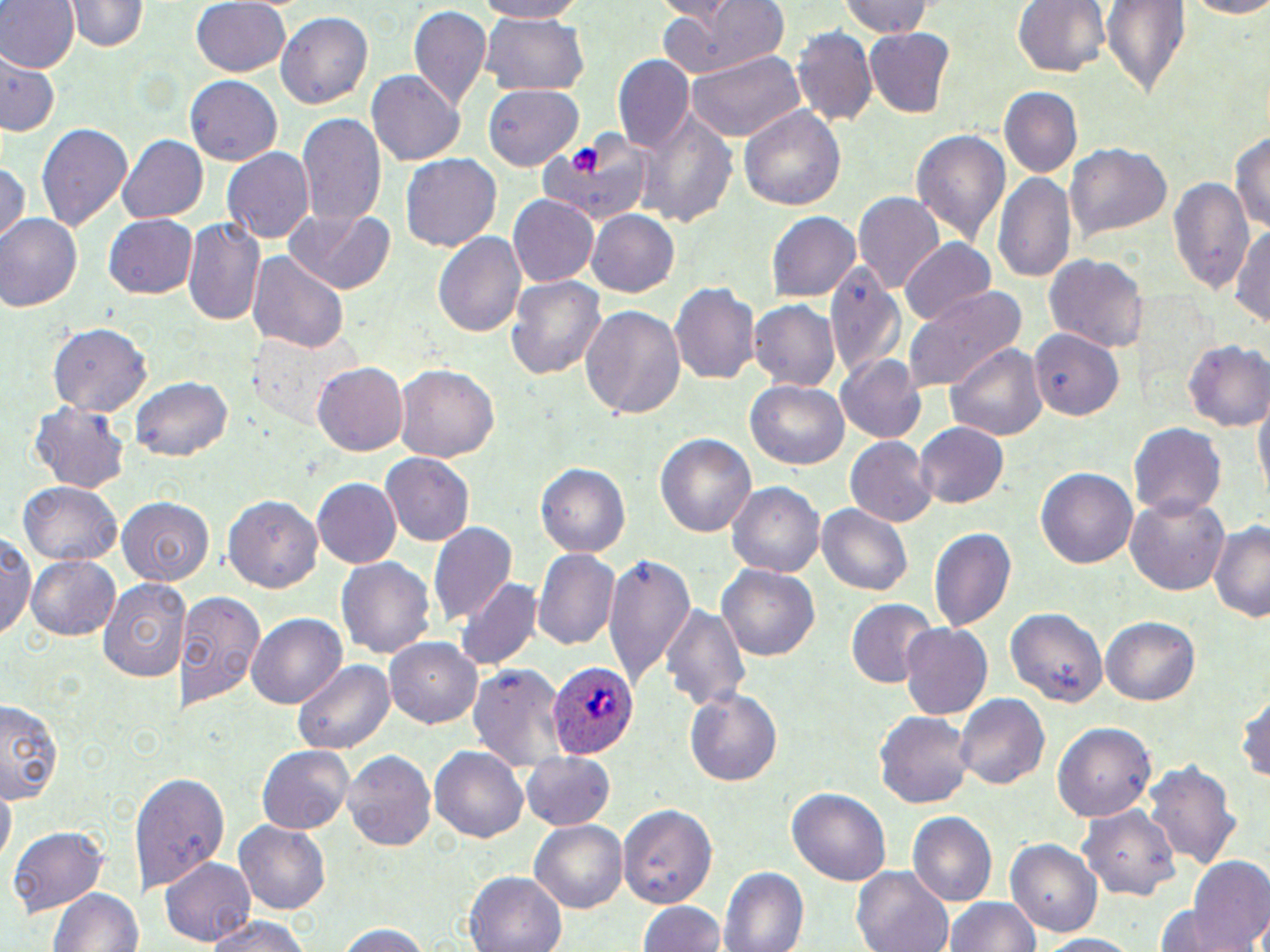

Summary:
  - Coordinate format: approximate bounding boxes as (x1, y1, x2, y2) in pixels
  - Platelet locations: (571, 144, 603, 176)
  - Plasmodium ovale-infected red blood cell locations: (546, 659, 638, 756)
  - Uninfected red blood cell locations: (0, 0, 78, 74), (65, 0, 150, 54), (193, 0, 292, 76), (473, 0, 590, 22), (837, 0, 934, 40), (1012, 0, 1108, 79), (1173, 0, 1270, 17), (1101, 1, 1192, 101), (655, 2, 792, 77), (408, 6, 493, 113), (276, 11, 372, 111), (479, 13, 587, 92), (793, 26, 878, 127), (865, 29, 956, 118), (684, 48, 808, 141), (614, 56, 695, 154), (3, 57, 58, 136), (367, 69, 466, 166), (185, 77, 283, 166), (483, 82, 582, 172), (997, 87, 1083, 181), (737, 104, 848, 214), (641, 107, 737, 229), (297, 113, 387, 231), (36, 122, 133, 235), (1232, 127, 1270, 241), (911, 130, 1011, 251), (117, 134, 209, 225), (535, 135, 656, 223), (1066, 143, 1172, 241), (223, 147, 314, 244), (402, 154, 500, 252), (0, 160, 28, 246), (994, 169, 1076, 286), (1170, 174, 1254, 299), (852, 192, 942, 295), (507, 195, 598, 287), (282, 207, 398, 294), (586, 209, 679, 298), (768, 211, 862, 302), (0, 215, 81, 312), (104, 215, 198, 299), (185, 219, 263, 327), (1231, 223, 1270, 333), (434, 230, 527, 339), (899, 238, 997, 328), (248, 253, 350, 354), (1044, 254, 1145, 352), (827, 259, 906, 384), (505, 275, 608, 384), (670, 284, 759, 382), (904, 285, 1025, 394), (750, 299, 843, 390), (581, 304, 687, 419), (48, 324, 154, 418), (1029, 329, 1124, 422), (253, 337, 349, 428), (1183, 340, 1268, 429), (948, 342, 1046, 444), (835, 352, 928, 442), (313, 362, 408, 455), (394, 363, 499, 462), (130, 375, 232, 460), (746, 381, 848, 471), (1252, 393, 1270, 507), (28, 403, 131, 492), (916, 423, 1009, 507), (1128, 424, 1226, 522), (653, 431, 756, 543), (845, 436, 937, 527), (382, 453, 474, 547), (535, 461, 632, 559), (1036, 467, 1138, 572), (311, 479, 402, 568), (16, 481, 124, 565), (729, 481, 826, 579), (117, 494, 215, 583), (226, 494, 324, 594), (1126, 495, 1232, 596), (817, 505, 913, 599), (1207, 517, 1270, 624), (427, 520, 516, 626), (929, 527, 1017, 634), (2, 534, 39, 644), (534, 548, 619, 653), (603, 552, 696, 690), (25, 554, 120, 641), (336, 554, 437, 658), (717, 564, 820, 666), (97, 575, 191, 683), (456, 578, 541, 672), (176, 589, 268, 713), (845, 600, 939, 692), (660, 602, 751, 719), (1006, 607, 1107, 708), (246, 614, 344, 710), (1101, 616, 1199, 707), (898, 622, 992, 721), (386, 636, 483, 726), (294, 659, 393, 757), (466, 664, 565, 769), (684, 686, 784, 787), (1236, 686, 1269, 787), (954, 695, 1049, 789), (0, 700, 65, 805), (874, 711, 973, 809), (1054, 724, 1157, 822), (257, 744, 353, 833), (430, 745, 529, 844), (343, 749, 436, 852), (521, 752, 615, 830), (1142, 761, 1241, 867), (132, 770, 230, 895), (0, 785, 15, 859), (787, 786, 891, 889), (617, 800, 718, 910), (1078, 806, 1182, 901), (907, 812, 998, 907), (234, 820, 332, 917), (530, 820, 626, 915), (8, 826, 109, 917), (1007, 838, 1102, 939), (1188, 855, 1270, 952), (159, 857, 255, 946), (853, 865, 955, 952), (721, 866, 813, 952), (466, 870, 568, 952), (49, 886, 142, 952), (946, 897, 1041, 952), (638, 900, 724, 952), (1150, 907, 1245, 952), (203, 915, 315, 952), (335, 922, 434, 952), (1031, 934, 1148, 951)
  - Slide-level diagnosis: Plasmodium ovale
  - Stain: May-Grünwald-Giemsa
  - Modality: light microscopy
  - Magnification: 1000x
  - Image size: 1270×952 pixels
  - Preparation: thin blood smear
  - Field of view: single